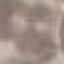
Result: no malaria parasites seen. Giemsa stain. Automatically extracted cell patch, resized to 64 × 64 pixels. Acquired by smartphone through the microscope eyepiece. Thin blood smear.